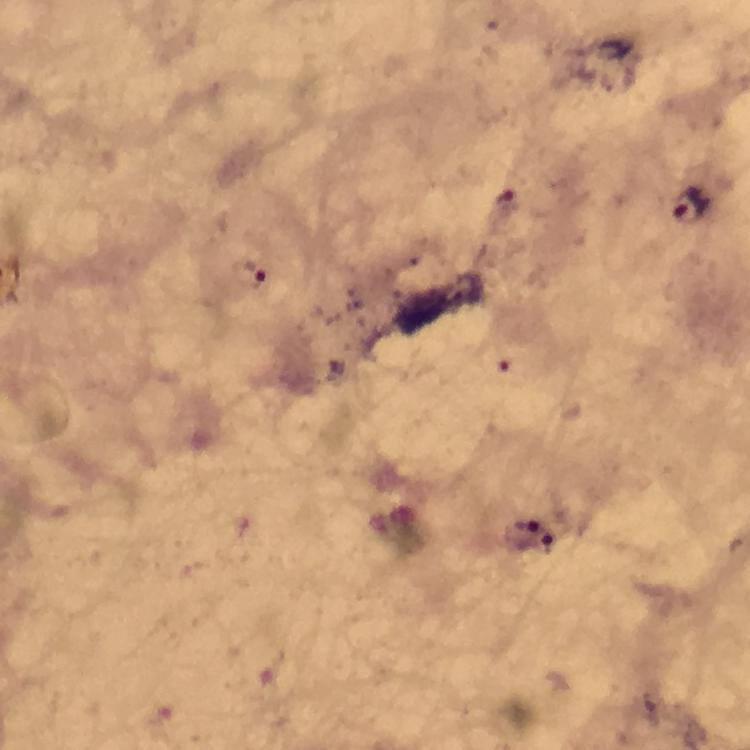

immersion oil = used
cropped from = a single field of view
stain = Giemsa
preparation = thick blood film
malaria parasite locations = approximate centers as {x, y} in pixels: {505, 198}, {691, 204}
context = from a diagnostic examination for malaria
image size = 750×750 pixels
capture = smartphone camera through the microscope
magnification = 100x